Report the malaria status of this cell.
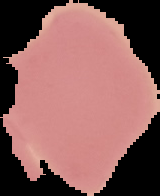

It is uninfected.

Image is 160×196 pixels. Cell region segmented out of the field of view; the surrounding area is masked to black. From a thin blood smear.